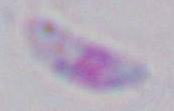

modality = micrograph
identification = Toxoplasma gondii
magnification = 1000x